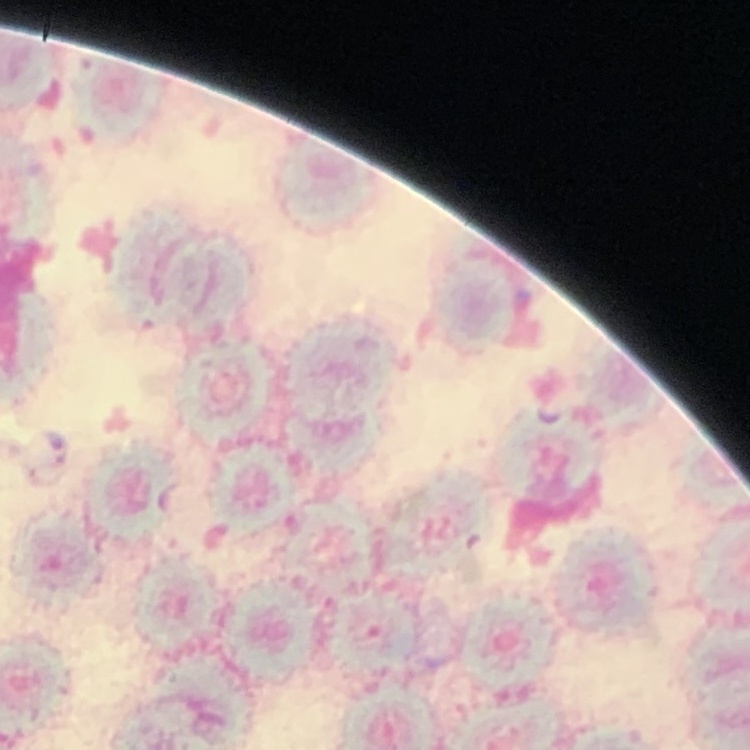

Summary:
  - Erythrocyte morphology: rouleaux formation
  - Preparation: thin blood smear
  - Stain: Field's or Giemsa
  - Image type: square crop of a larger photomicrograph